State which parasite is depicted.
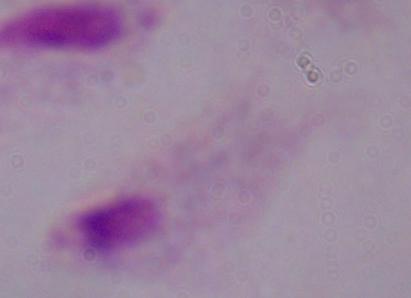

This is a trichomonad.

Micrograph. 1000x magnification.